Describe the morphology of the red blood cells.
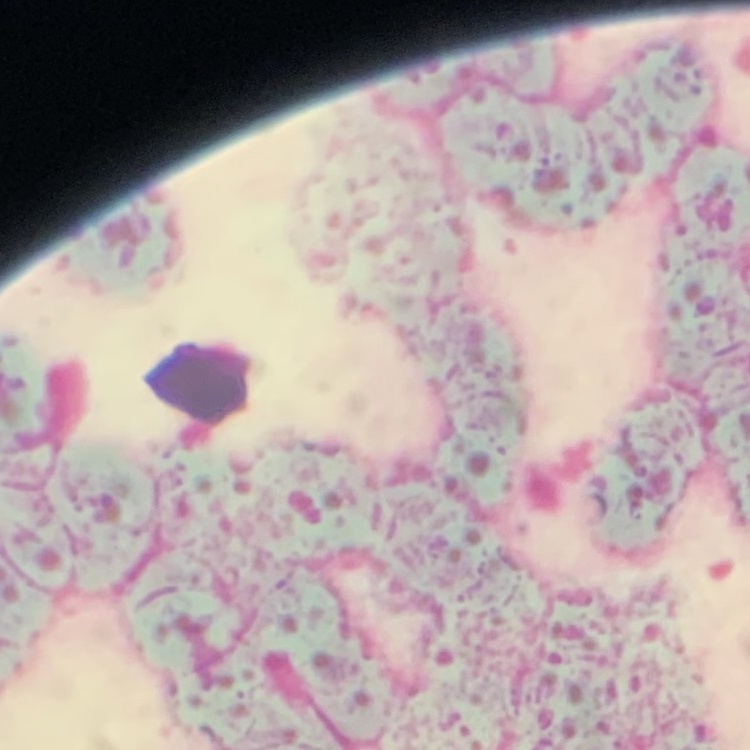
Rouleaux formation.

preparation = thin peripheral smear
image type = square crop of a larger photomicrograph
stain = Field's or Giemsa